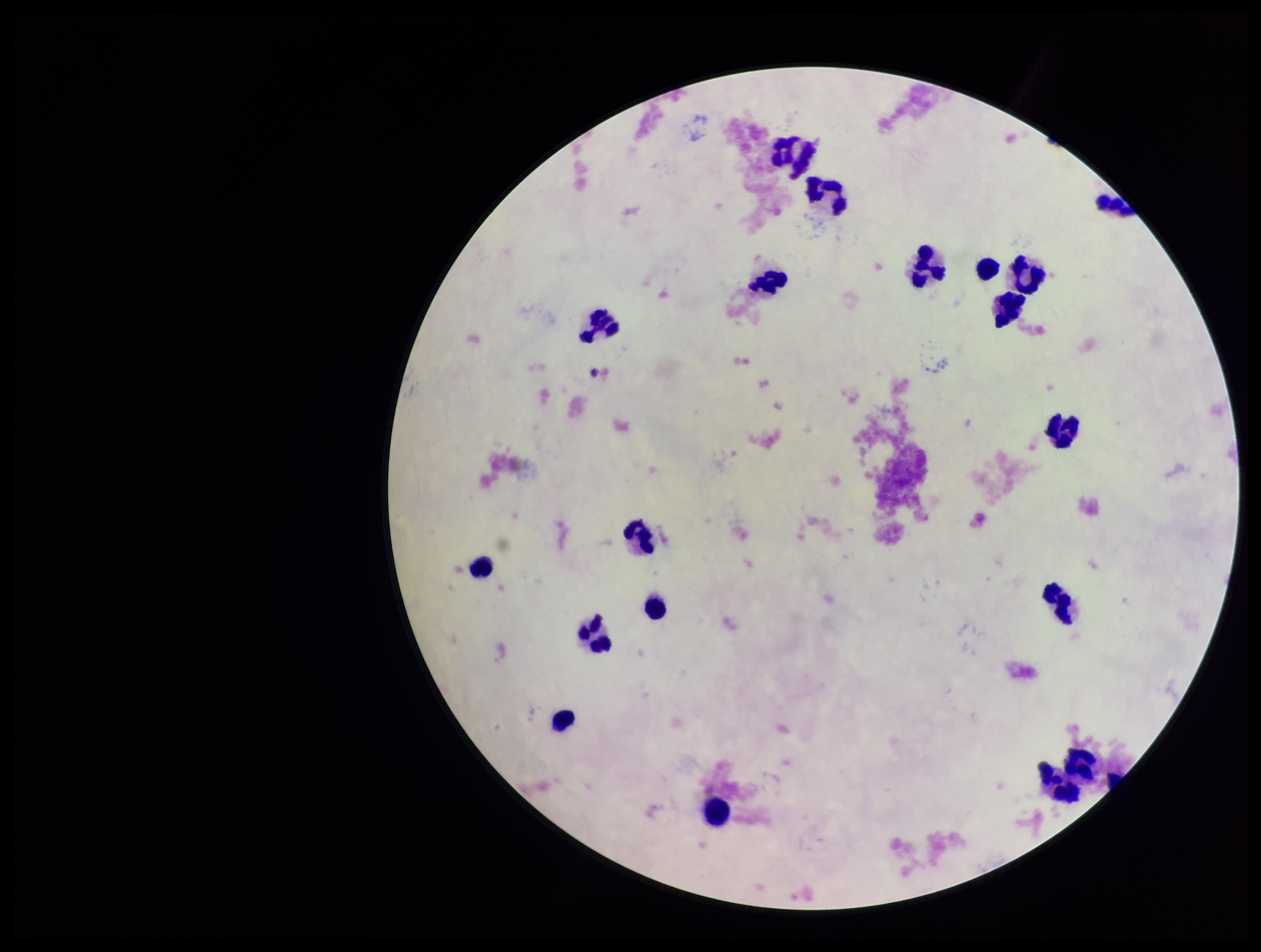
Summary:
  - Parasite count: 0
  - Stain: Giemsa
  - Patient malaria status: negative
  - Field of view: one from this slide
  - Preparation: thick smear
  - Capture: smartphone photograph through the microscope eyepiece
  - Image size: 1261×952 pixels
  - Leukocyte count: 19
  - Plasmodium parasites: none detected